Classify this cell by malaria status.
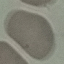

It is uninfected.

Acquired by smartphone through the microscope eyepiece. Thin smear of blood. Giemsa-stained preparation. Cell patch, automatically extracted from a larger field of view and resized to 64 × 64 pixels.